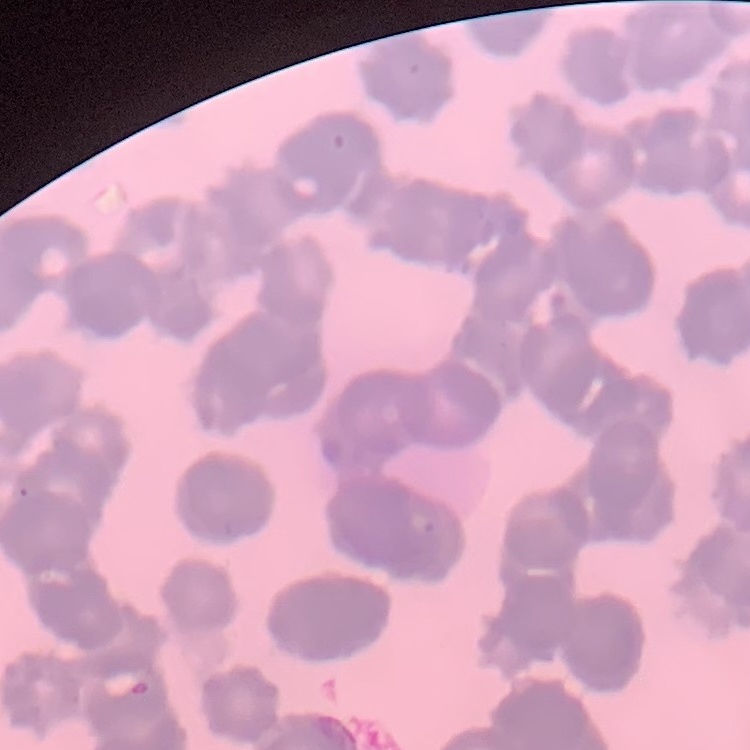

Summary:
  - Erythrocyte morphology: rouleaux formation
  - Image type: one tile cut from a larger photomicrograph
  - Preparation: thin blood smear
  - Stain: Field's or Giemsa